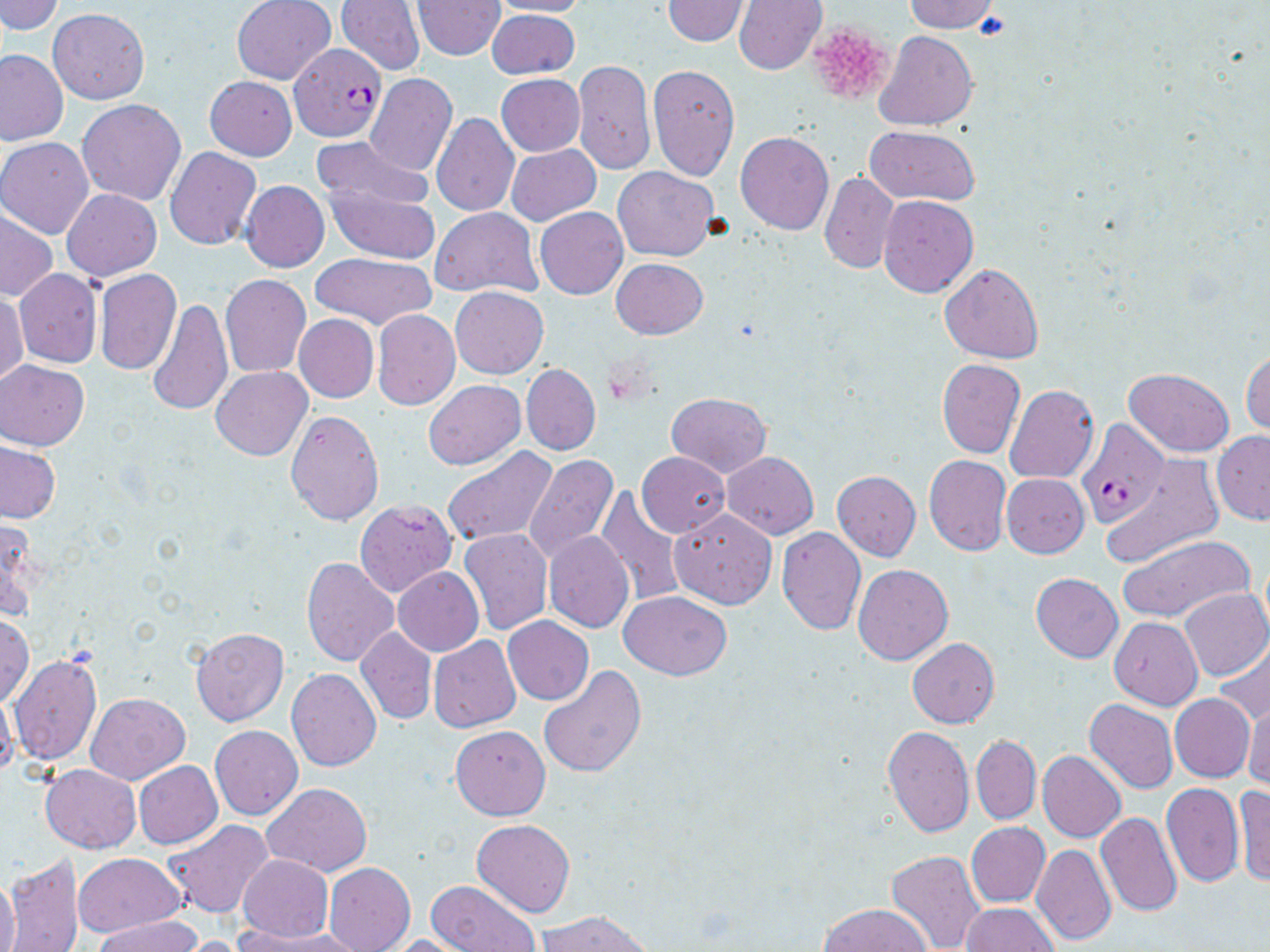 Approximate bounding boxes as (x1, y1, x2, y2) in pixels. Plasmodium falciparum-infected red blood cell locations: (289, 42, 387, 143), (1076, 418, 1166, 529). Platelet locations: (808, 20, 895, 106). Uninfected red blood cell locations: (1, 0, 63, 36), (231, 0, 336, 84), (336, 0, 424, 75), (413, 0, 506, 60), (491, 0, 590, 17), (662, 0, 750, 46), (734, 0, 827, 74), (902, 0, 1002, 34), (48, 9, 149, 104), (486, 9, 579, 79), (874, 30, 979, 130), (0, 48, 67, 145), (572, 60, 655, 177), (648, 64, 739, 180), (365, 73, 458, 177), (496, 75, 584, 156), (205, 76, 296, 160), (77, 99, 186, 205), (431, 113, 519, 215), (863, 124, 981, 205), (736, 131, 834, 235), (310, 135, 431, 215), (0, 139, 93, 238), (505, 144, 601, 227), (165, 146, 260, 250), (613, 166, 718, 261), (819, 172, 899, 275), (240, 180, 329, 272), (328, 185, 440, 263), (61, 188, 162, 281), (877, 195, 978, 298), (536, 207, 629, 299), (430, 208, 542, 297), (1, 209, 56, 302), (311, 253, 436, 330), (611, 258, 707, 339), (939, 263, 1045, 363), (14, 269, 102, 368), (94, 269, 181, 374), (220, 275, 311, 376), (450, 286, 549, 379), (1, 292, 28, 384), (145, 296, 232, 417), (372, 309, 460, 411), (294, 314, 379, 403), (1241, 348, 1270, 437), (937, 358, 1025, 459), (1, 360, 88, 450), (521, 363, 600, 455), (211, 366, 312, 460), (1124, 368, 1234, 457), (422, 380, 525, 470), (1005, 384, 1099, 483), (666, 392, 772, 477), (286, 409, 384, 527), (1213, 431, 1270, 524), (0, 442, 60, 523), (440, 446, 558, 547), (637, 452, 729, 537), (722, 452, 819, 538), (522, 454, 619, 563), (924, 454, 1010, 556), (1101, 457, 1223, 566), (832, 471, 921, 560), (1001, 473, 1089, 558), (596, 487, 686, 607), (355, 500, 457, 597), (670, 509, 778, 609), (0, 516, 42, 623), (319, 516, 419, 639), (457, 528, 552, 634), (776, 528, 866, 635), (543, 532, 634, 633), (1118, 534, 1253, 626), (302, 556, 398, 667), (851, 564, 953, 665), (394, 567, 484, 655), (1031, 573, 1123, 663), (1180, 587, 1270, 682), (618, 591, 732, 679), (1, 612, 34, 709), (503, 616, 593, 704), (1109, 617, 1202, 709), (190, 627, 290, 727), (355, 628, 437, 724), (429, 636, 520, 732), (907, 638, 999, 728), (1212, 639, 1270, 727), (7, 653, 103, 765), (537, 666, 647, 778), (287, 668, 382, 770), (0, 690, 18, 782), (84, 692, 189, 785), (1170, 694, 1254, 781), (1242, 695, 1270, 791), (1084, 698, 1177, 794), (451, 725, 550, 820), (210, 726, 303, 820), (881, 727, 974, 837), (971, 736, 1041, 825), (1037, 750, 1126, 842), (134, 761, 223, 849), (40, 764, 141, 853), (1161, 782, 1244, 888), (262, 783, 373, 875), (1232, 784, 1270, 889), (246, 788, 354, 937), (1094, 811, 1182, 916), (163, 819, 274, 918), (471, 819, 575, 917), (966, 822, 1049, 908), (1032, 844, 1116, 946), (885, 849, 985, 952), (74, 852, 186, 937), (3, 853, 85, 952), (237, 855, 333, 941), (324, 862, 415, 952), (0, 872, 20, 952), (426, 881, 540, 951), (818, 903, 931, 952), (962, 903, 1057, 952), (536, 910, 655, 952), (92, 916, 203, 951), (231, 925, 359, 952), (385, 934, 474, 952), (171, 936, 254, 952). Slide-level diagnosis: Plasmodium falciparum. Optical microscopy. Captured at 1000x magnification. Image is 1270×952 pixels. May-Grünwald-Giemsa-stained preparation. Single field of view. Thin blood smear.